Report the malaria status of this cell.
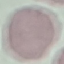
Uninfected.

Summary:
  - Stain: Giemsa
  - Capture: smartphone through the microscope eyepiece
  - Image type: automatically extracted cell patch, resized to 64 × 64 pixels
  - Preparation: thin blood film